Report the malaria status of this cell.
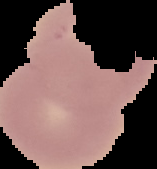

Uninfected.

Summary:
  - Preparation: thin blood film
  - Image size: 157×169 pixels
  - Image type: cell region segmented out of the field of view; surrounding area masked to black